Locate every blood parasite and identify its species.
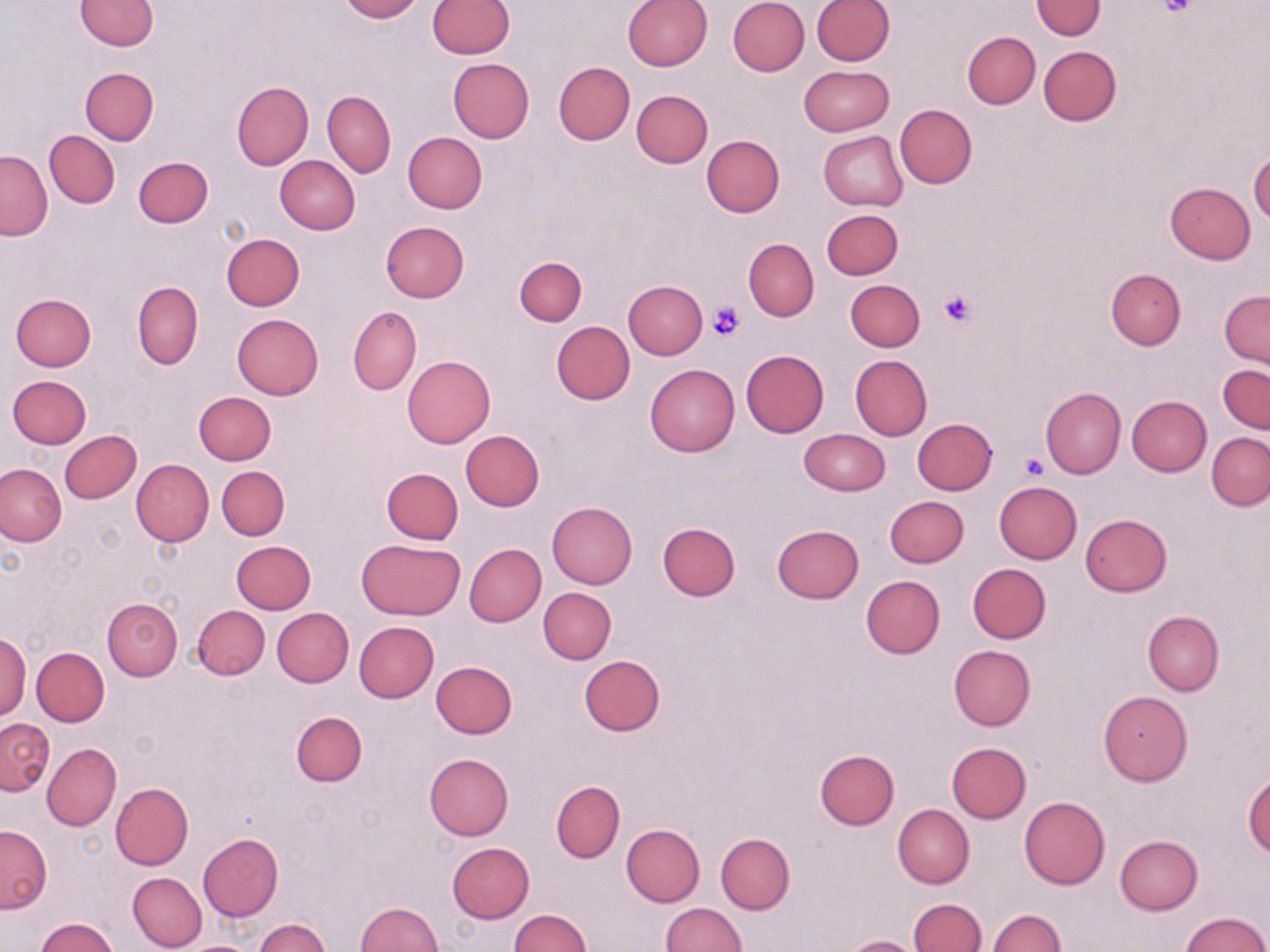
No blood parasites observed.

Summary:
  - Coordinate format: approximate bounding boxes as named x1/y1/x2/y2 corners in pixels
  - Uninfected red blood cell locations: (x1=74, y1=0, x2=159, y2=50), (x1=339, y1=0, x2=423, y2=22), (x1=623, y1=0, x2=712, y2=72), (x1=728, y1=0, x2=809, y2=76), (x1=811, y1=0, x2=894, y2=66), (x1=427, y1=1, x2=513, y2=58), (x1=1031, y1=1, x2=1105, y2=39), (x1=962, y1=31, x2=1039, y2=109), (x1=1038, y1=46, x2=1121, y2=126), (x1=448, y1=58, x2=533, y2=143), (x1=552, y1=61, x2=635, y2=144), (x1=798, y1=65, x2=894, y2=136), (x1=80, y1=67, x2=159, y2=145), (x1=233, y1=82, x2=314, y2=170), (x1=323, y1=90, x2=396, y2=176), (x1=632, y1=90, x2=712, y2=168), (x1=894, y1=104, x2=976, y2=189), (x1=45, y1=131, x2=119, y2=207), (x1=819, y1=131, x2=907, y2=210), (x1=403, y1=132, x2=487, y2=213), (x1=701, y1=135, x2=784, y2=218), (x1=1, y1=151, x2=51, y2=239), (x1=1248, y1=151, x2=1270, y2=224), (x1=275, y1=155, x2=361, y2=234), (x1=134, y1=156, x2=213, y2=227), (x1=1164, y1=183, x2=1255, y2=265), (x1=820, y1=208, x2=903, y2=279), (x1=380, y1=221, x2=469, y2=303), (x1=221, y1=233, x2=304, y2=310), (x1=743, y1=239, x2=819, y2=321), (x1=515, y1=256, x2=587, y2=325), (x1=1106, y1=269, x2=1186, y2=349), (x1=845, y1=279, x2=924, y2=351), (x1=132, y1=280, x2=203, y2=369), (x1=623, y1=280, x2=706, y2=360), (x1=1220, y1=290, x2=1269, y2=369), (x1=11, y1=292, x2=96, y2=371), (x1=348, y1=306, x2=421, y2=396), (x1=231, y1=313, x2=323, y2=399), (x1=550, y1=320, x2=635, y2=404), (x1=740, y1=349, x2=829, y2=437), (x1=850, y1=355, x2=932, y2=439), (x1=402, y1=356, x2=495, y2=447), (x1=645, y1=364, x2=740, y2=457), (x1=1218, y1=364, x2=1270, y2=434), (x1=9, y1=374, x2=92, y2=448), (x1=1040, y1=386, x2=1125, y2=478), (x1=194, y1=391, x2=276, y2=465), (x1=1126, y1=396, x2=1212, y2=476), (x1=913, y1=418, x2=997, y2=494), (x1=798, y1=428, x2=888, y2=496), (x1=60, y1=431, x2=141, y2=504), (x1=461, y1=431, x2=545, y2=511), (x1=1207, y1=433, x2=1270, y2=510), (x1=130, y1=459, x2=213, y2=546), (x1=0, y1=464, x2=66, y2=546), (x1=217, y1=466, x2=289, y2=540), (x1=381, y1=467, x2=463, y2=544), (x1=994, y1=480, x2=1081, y2=563), (x1=884, y1=495, x2=968, y2=567), (x1=547, y1=501, x2=637, y2=588), (x1=1080, y1=513, x2=1172, y2=596), (x1=657, y1=523, x2=740, y2=600), (x1=771, y1=524, x2=865, y2=604), (x1=356, y1=538, x2=465, y2=620), (x1=361, y1=540, x2=452, y2=704), (x1=232, y1=541, x2=316, y2=613), (x1=464, y1=543, x2=546, y2=627), (x1=967, y1=563, x2=1051, y2=643), (x1=860, y1=575, x2=945, y2=659), (x1=538, y1=587, x2=616, y2=664), (x1=103, y1=598, x2=182, y2=680), (x1=193, y1=604, x2=270, y2=680), (x1=272, y1=607, x2=354, y2=687), (x1=1143, y1=610, x2=1223, y2=696), (x1=354, y1=622, x2=439, y2=703), (x1=0, y1=631, x2=31, y2=721), (x1=948, y1=644, x2=1036, y2=730), (x1=31, y1=647, x2=109, y2=726), (x1=579, y1=655, x2=665, y2=735), (x1=431, y1=661, x2=517, y2=738), (x1=1098, y1=690, x2=1192, y2=786), (x1=290, y1=712, x2=367, y2=787), (x1=1, y1=718, x2=54, y2=794), (x1=947, y1=742, x2=1030, y2=822), (x1=43, y1=743, x2=121, y2=831), (x1=814, y1=749, x2=899, y2=829), (x1=425, y1=753, x2=514, y2=840), (x1=1242, y1=773, x2=1270, y2=859), (x1=552, y1=780, x2=625, y2=862), (x1=110, y1=782, x2=193, y2=870), (x1=1019, y1=796, x2=1110, y2=889), (x1=893, y1=804, x2=973, y2=888), (x1=621, y1=824, x2=705, y2=907), (x1=0, y1=825, x2=52, y2=913), (x1=198, y1=833, x2=284, y2=921), (x1=716, y1=833, x2=795, y2=915), (x1=1115, y1=835, x2=1203, y2=914), (x1=446, y1=842, x2=535, y2=924), (x1=128, y1=873, x2=206, y2=950), (x1=909, y1=899, x2=986, y2=952), (x1=354, y1=901, x2=443, y2=952), (x1=661, y1=902, x2=747, y2=951), (x1=507, y1=909, x2=591, y2=951), (x1=987, y1=909, x2=1067, y2=951), (x1=1181, y1=912, x2=1268, y2=951), (x1=32, y1=917, x2=121, y2=952), (x1=253, y1=917, x2=330, y2=951), (x1=843, y1=935, x2=921, y2=952), (x1=177, y1=939, x2=265, y2=952)
  - Platelet locations: (x1=1158, y1=0, x2=1197, y2=16), (x1=938, y1=289, x2=975, y2=329), (x1=709, y1=301, x2=746, y2=340), (x1=1020, y1=452, x2=1048, y2=480)
  - Slide-level diagnosis: negative for blood parasites
  - Modality: optical microscopy
  - Field of view: single
  - Image size: 1270×952 pixels
  - Stain: May-Grünwald-Giemsa
  - Preparation: thin blood film
  - Magnification: 1000x